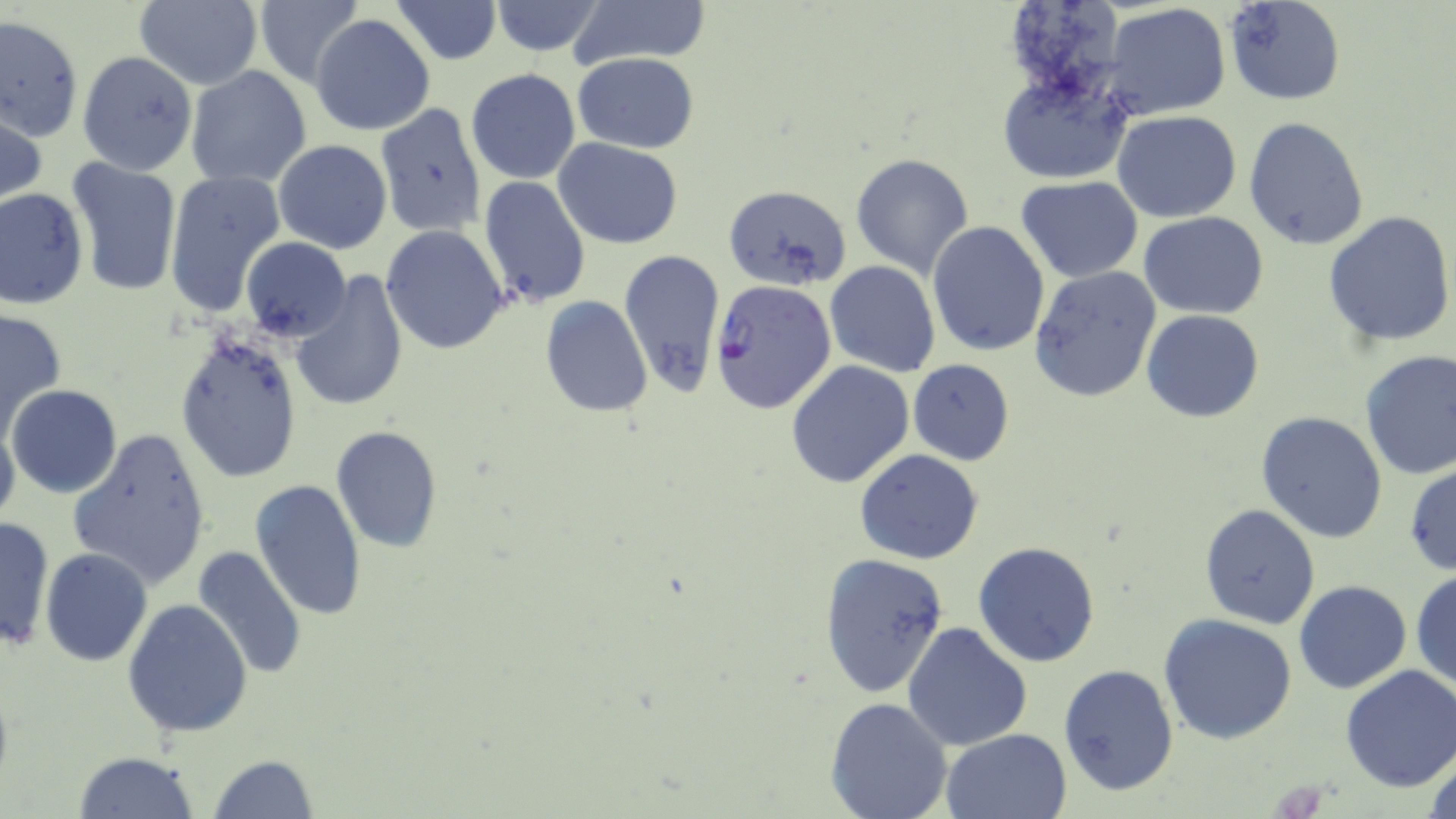
slide_level_diagnosis: Plasmodium falciparum
uninfected_red_blood_cell_locations: 'approximate bounding boxes as named x1/y1/x2/y2 corners in pixels: (x1=252, y1=0, x2=365, y2=88), (x1=389, y1=0, x2=503, y2=64), (x1=571, y1=0, x2=710, y2=70), (x1=133, y1=1, x2=264, y2=89), (x1=488, y1=1, x2=607, y2=56), (x1=1224, y1=1, x2=1345, y2=106), (x1=1101, y1=2, x2=1232, y2=121), (x1=0, y1=13, x2=83, y2=144), (x1=311, y1=14, x2=435, y2=136), (x1=76, y1=51, x2=197, y2=175), (x1=573, y1=53, x2=697, y2=154), (x1=186, y1=66, x2=311, y2=188), (x1=994, y1=67, x2=1136, y2=189), (x1=466, y1=68, x2=580, y2=183), (x1=371, y1=105, x2=489, y2=239), (x1=1, y1=106, x2=47, y2=209), (x1=1112, y1=111, x2=1241, y2=223), (x1=1243, y1=117, x2=1369, y2=252), (x1=555, y1=138, x2=683, y2=249), (x1=274, y1=139, x2=392, y2=254), (x1=851, y1=153, x2=974, y2=278), (x1=65, y1=157, x2=182, y2=297), (x1=164, y1=169, x2=285, y2=317), (x1=478, y1=176, x2=591, y2=307), (x1=1016, y1=177, x2=1143, y2=282), (x1=724, y1=184, x2=852, y2=291), (x1=0, y1=187, x2=88, y2=311), (x1=1139, y1=210, x2=1269, y2=320), (x1=1324, y1=210, x2=1456, y2=346), (x1=929, y1=220, x2=1052, y2=358), (x1=380, y1=225, x2=510, y2=353), (x1=241, y1=236, x2=351, y2=341), (x1=618, y1=248, x2=727, y2=398), (x1=824, y1=261, x2=940, y2=378), (x1=1029, y1=265, x2=1162, y2=402), (x1=289, y1=273, x2=411, y2=413), (x1=539, y1=296, x2=652, y2=418), (x1=0, y1=306, x2=68, y2=438), (x1=1141, y1=310, x2=1264, y2=424), (x1=175, y1=330, x2=303, y2=483), (x1=1359, y1=351, x2=1456, y2=480), (x1=907, y1=360, x2=1015, y2=465), (x1=786, y1=361, x2=914, y2=486), (x1=7, y1=384, x2=123, y2=499), (x1=1256, y1=411, x2=1388, y2=543), (x1=0, y1=418, x2=20, y2=532), (x1=330, y1=425, x2=444, y2=552), (x1=68, y1=427, x2=213, y2=590), (x1=854, y1=449, x2=984, y2=564), (x1=1405, y1=461, x2=1456, y2=578), (x1=249, y1=480, x2=368, y2=622), (x1=1198, y1=503, x2=1322, y2=630), (x1=0, y1=516, x2=55, y2=652), (x1=973, y1=540, x2=1101, y2=668), (x1=191, y1=546, x2=308, y2=681), (x1=41, y1=548, x2=152, y2=666), (x1=818, y1=553, x2=950, y2=697), (x1=1412, y1=570, x2=1456, y2=695), (x1=1293, y1=580, x2=1412, y2=695), (x1=122, y1=599, x2=252, y2=740), (x1=1158, y1=613, x2=1297, y2=743), (x1=903, y1=622, x2=1033, y2=751), (x1=1058, y1=663, x2=1178, y2=796), (x1=1338, y1=666, x2=1456, y2=792), (x1=825, y1=697, x2=953, y2=819), (x1=940, y1=729, x2=1071, y2=817), (x1=1423, y1=741, x2=1456, y2=819), (x1=74, y1=750, x2=198, y2=818), (x1=208, y1=755, x2=321, y2=818)'
stain: May-Grünwald-Giemsa
magnification: 1000x
plasmodium_falciparum_infected_red_blood_cell_locations: 'approximate bounding boxes as named x1/y1/x2/y2 corners in pixels: (x1=710, y1=280, x2=837, y2=414)'
image_size: 1456×819 pixels
preparation: thin blood smear
modality: light microscopy
field_of_view: single